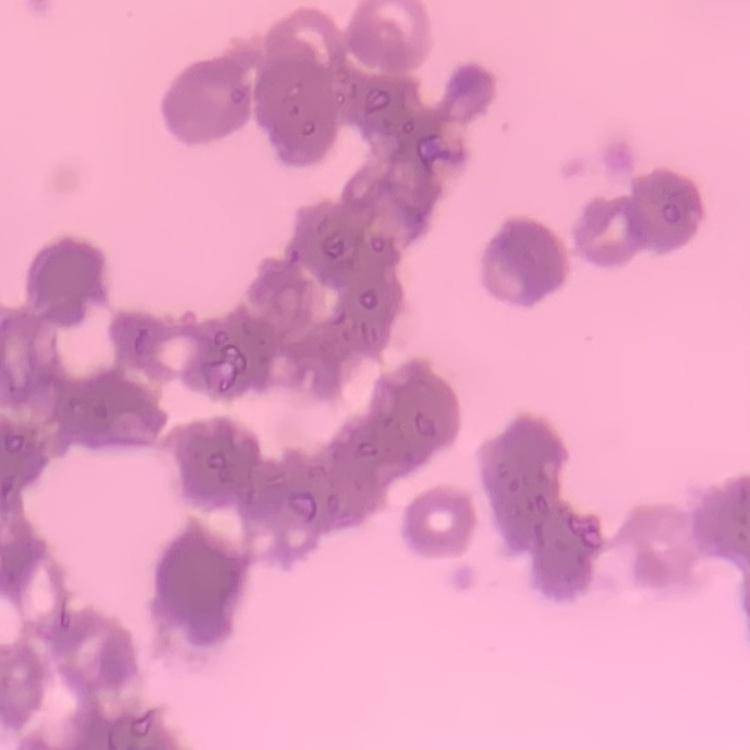

The erythrocytes show rouleaux formation. Square crop of a larger photomicrograph. Field's or Giemsa stain. Thin blood film.